Report the malaria status of this cell.
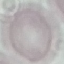
It is uninfected.

{
  "image_type": "automatically extracted cell patch, resized to 64 × 64 pixels",
  "capture": "smartphone camera at the microscope eyepiece",
  "preparation": "thin blood smear",
  "stain": "Giemsa"
}